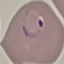

result = malaria parasites detected
stain = Giemsa
capture = smartphone through the microscope eyepiece
image type = cell patch, automatically extracted from a larger field of view and resized to 64 × 64 pixels
preparation = thin smear